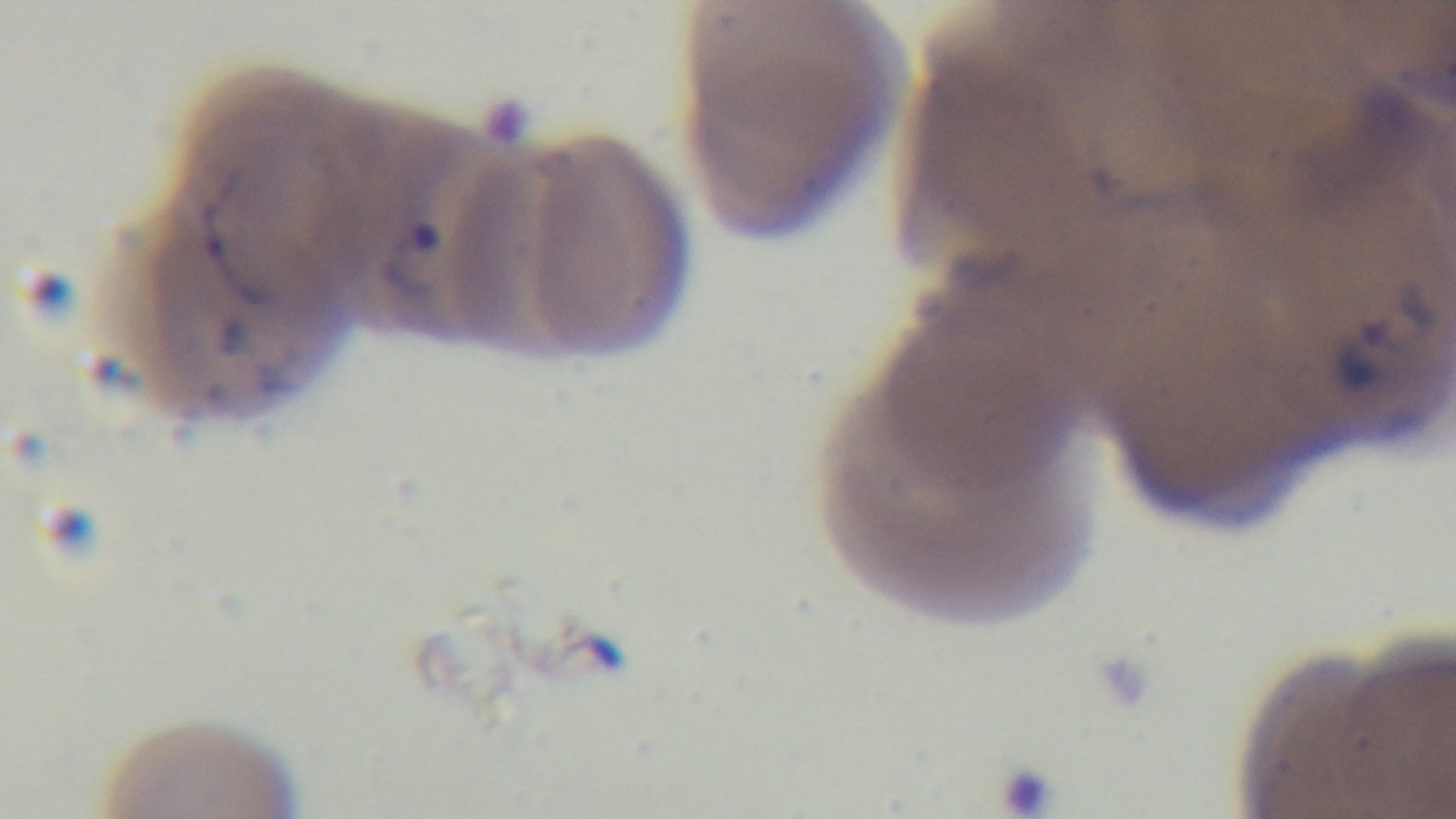
Summary:
  - Stain: Giemsa
  - Field of view: one from the slide
  - Capture: mounted 4K digital camera
  - Malaria status: positive
  - Modality: light microscopy
  - Objective: 100x oil immersion
  - Preparation: thin blood film